Comment on the morphology of the erythrocytes.
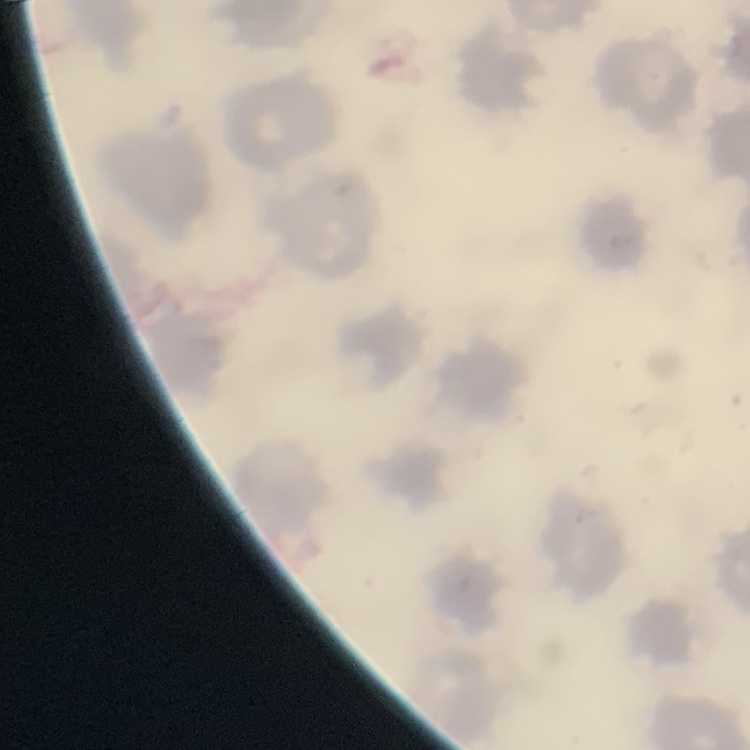
No rouleaux formation.

preparation = thin peripheral smear
image type = square crop of a larger photomicrograph
stain = Field's or Giemsa